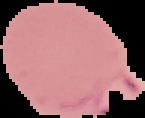
{
  "image_type": "segmented cell region with the area outside set to black",
  "malaria_status": "parasitized",
  "image_size": "145×118 pixels",
  "preparation": "thin blood smear"
}